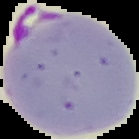
{
  "image_type": "cell region segmented out of the field of view; surrounding area masked to black",
  "preparation": "thin blood film",
  "malaria_status": "parasitized",
  "image_size": "139×139 pixels"
}